Give the position of every Plasmodium parasite visible.
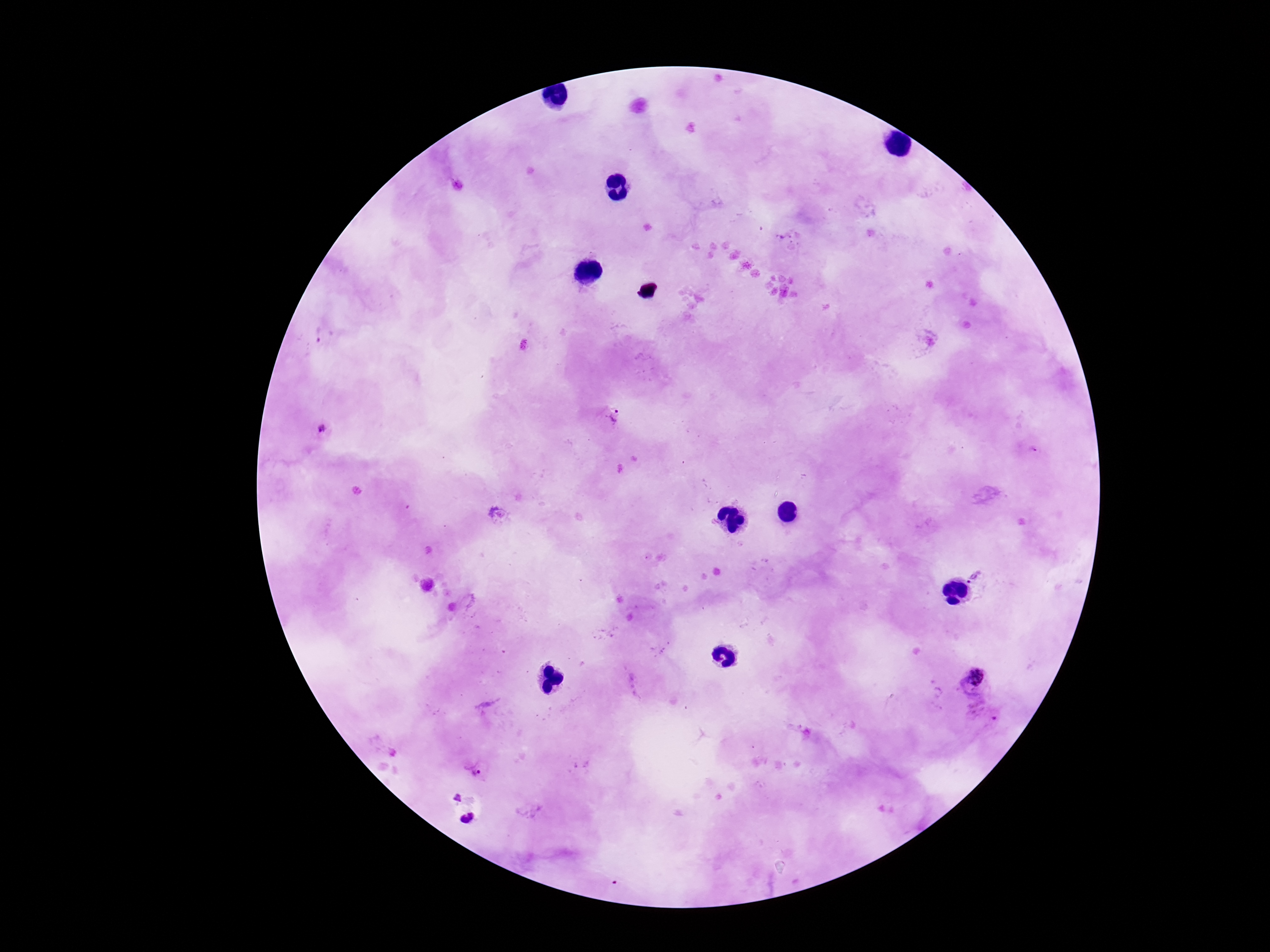
Approximate object centers, in pixels from the top-left corner.
Plasmodium parasites: (x=790, y=239), (x=324, y=336), (x=613, y=418), (x=323, y=431), (x=497, y=514), (x=977, y=576), (x=973, y=680), (x=984, y=713), (x=476, y=768).

{
  "stain": "Giemsa",
  "image_size": "1270×952 pixels",
  "preparation": "thick peripheral-blood smear",
  "capture": "smartphone camera through the microscope eyepiece",
  "patient_malaria_status": "positive",
  "magnification": "100x",
  "field_of_view": "one from this slide"
}